Locate every Plasmodium parasite.
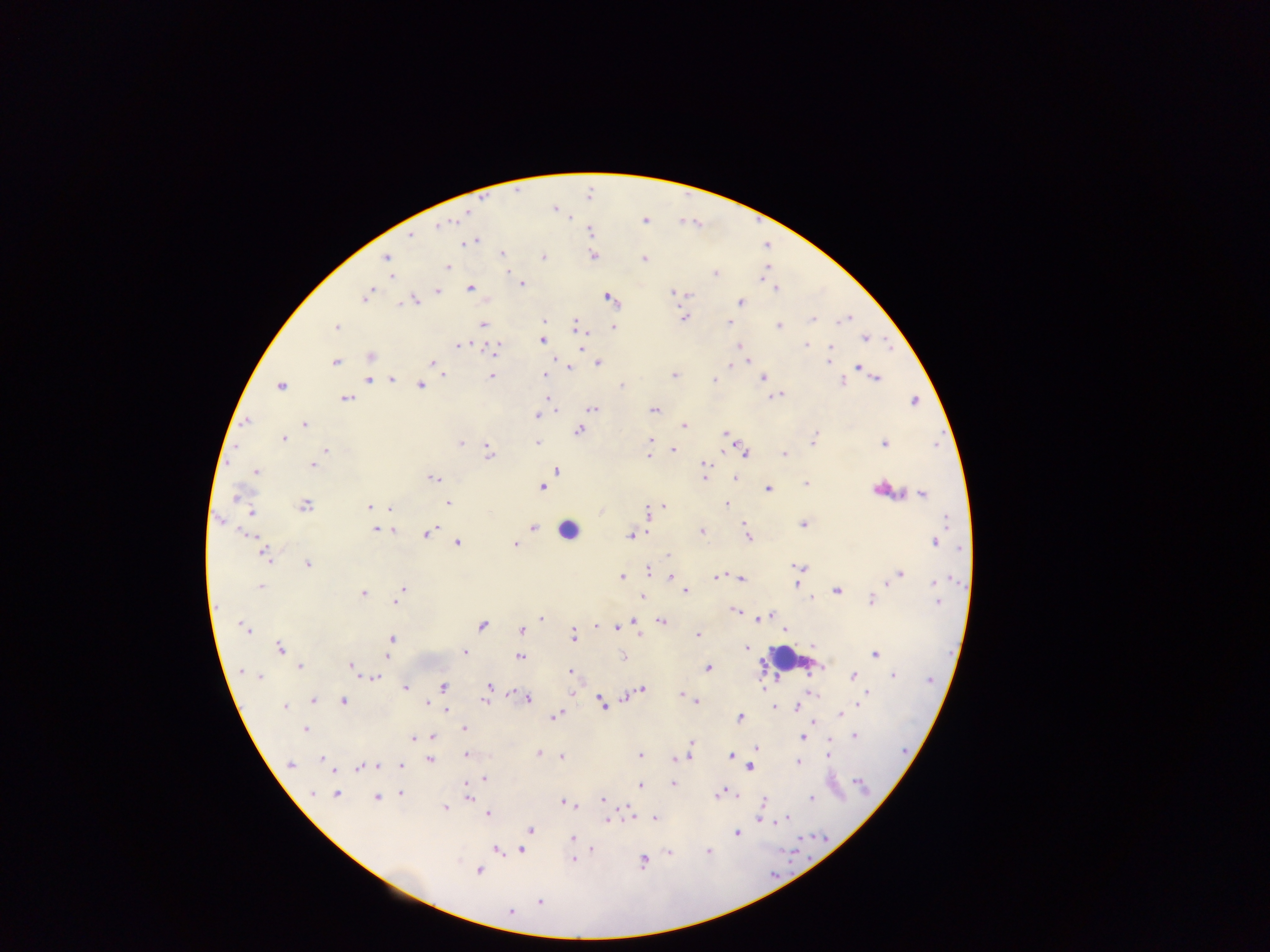
Approximate centers as {x, y} in pixels.
Plasmodium parasites: {554, 210}, {466, 212}, {568, 216}, {646, 220}, {438, 225}, {591, 231}, {409, 237}, {471, 242}, {502, 254}, {592, 256}, {385, 257}, {543, 258}, {644, 258}, {447, 266}, {716, 274}, {391, 276}, {520, 283}, {470, 288}, {775, 289}, {437, 290}, {673, 292}, {683, 294}, {365, 296}, {608, 297}, {414, 301}, {741, 302}, {683, 318}, {813, 319}, {843, 319}, {543, 320}, {729, 322}, {483, 324}, {575, 326}, {778, 326}, {336, 327}, {612, 327}, {865, 338}, {541, 340}, {806, 344}, {456, 345}, {738, 346}, {580, 347}, {828, 348}, {493, 350}, {370, 356}, {334, 361}, {748, 361}, {828, 362}, {432, 363}, {597, 364}, {731, 364}, {564, 365}, {858, 366}, {568, 368}, {673, 375}, {443, 376}, {491, 376}, {544, 376}, {876, 377}, {762, 378}, {714, 379}, {367, 380}, {392, 380}, {842, 382}, {280, 384}, {421, 385}, {622, 385}, {775, 396}, {345, 398}, {914, 401}, {553, 407}, {592, 409}, {654, 410}, {536, 415}, {246, 421}, {303, 424}, {683, 425}, {579, 430}, {726, 433}, {283, 438}, {650, 440}, {812, 441}, {460, 442}, {537, 442}, {883, 443}, {325, 450}, {672, 450}, {725, 450}, {745, 451}, {489, 452}, {652, 454}, {783, 454}, {647, 456}, {313, 464}, {702, 464}, {556, 470}, {255, 472}, {434, 478}, {703, 478}, {734, 478}, {806, 484}, {541, 487}, {881, 487}, {767, 488}, {922, 493}, {239, 497}, {447, 503}, {726, 504}, {305, 505}, {664, 505}, {369, 507}, {391, 507}, {251, 511}, {647, 513}, {219, 521}, {743, 522}, {803, 524}, {534, 527}, {376, 529}, {391, 529}, {700, 531}, {426, 532}, {646, 532}, {250, 535}, {630, 535}, {747, 536}, {458, 542}, {934, 542}, {515, 544}, {265, 554}, {668, 555}, {308, 564}, {801, 567}, {647, 570}, {899, 574}, {622, 576}, {670, 576}, {718, 577}, {741, 578}, {934, 580}, {886, 582}, {796, 584}, {260, 586}, {402, 590}, {836, 590}, {685, 591}, {362, 593}, {640, 596}, {812, 598}, {397, 599}, {871, 600}, {938, 602}, {736, 611}, {772, 614}, {542, 618}, {757, 619}, {661, 621}, {633, 623}, {481, 625}, {597, 626}, {246, 627}, {620, 627}, {613, 628}, {521, 630}, {783, 630}, {697, 635}, {572, 636}, {391, 638}, {813, 645}, {746, 647}, {279, 648}, {465, 652}, {875, 654}, {387, 655}, {520, 656}, {622, 656}, {351, 664}, {301, 666}, {707, 667}, {241, 672}, {570, 672}, {893, 675}, {257, 676}, {373, 676}, {852, 677}, {406, 687}, {443, 687}, {488, 687}, {764, 687}, {642, 689}, {868, 692}, {571, 694}, {679, 695}, {684, 696}, {526, 698}, {624, 698}, {313, 699}, {343, 700}, {485, 700}, {426, 701}, {602, 701}, {695, 701}, {285, 706}, {797, 706}, {774, 708}, {446, 711}, {839, 714}, {553, 715}, {740, 717}, {812, 720}, {305, 728}, {463, 728}, {854, 735}, {432, 737}, {804, 737}, {414, 739}, {691, 743}, {827, 743}, {755, 748}, {538, 754}, {640, 755}, {466, 756}, {560, 756}, {731, 756}, {689, 757}, {828, 757}, {320, 758}, {673, 758}, {680, 758}, {429, 760}, {797, 761}, {289, 764}, {375, 765}, {401, 766}, {359, 767}, {751, 767}, {333, 772}, {484, 778}, {855, 781}, {466, 782}, {673, 783}, {640, 785}, {313, 793}, {401, 793}, {721, 793}, {335, 794}, {735, 795}, {376, 797}, {468, 797}, {811, 798}, {602, 799}, {762, 802}, {566, 803}, {445, 806}, {628, 811}, {487, 813}, {653, 818}, {759, 818}, {632, 819}, {788, 819}, {607, 820}, {772, 820}, {530, 829}, {737, 833}, {572, 839}, {496, 849}, {592, 849}, {521, 850}, {668, 852}, {709, 852}, {573, 860}, {643, 861}, {478, 870}, {539, 902}, {510, 911}.

Summary:
  - Leukocyte locations: {568, 529}, {790, 659}
  - Preparation: thick blood film
  - Image size: 1270×952 pixels
  - Field of view: single
  - Country: Ghana
  - Capture: mobile-phone photograph through a microscope